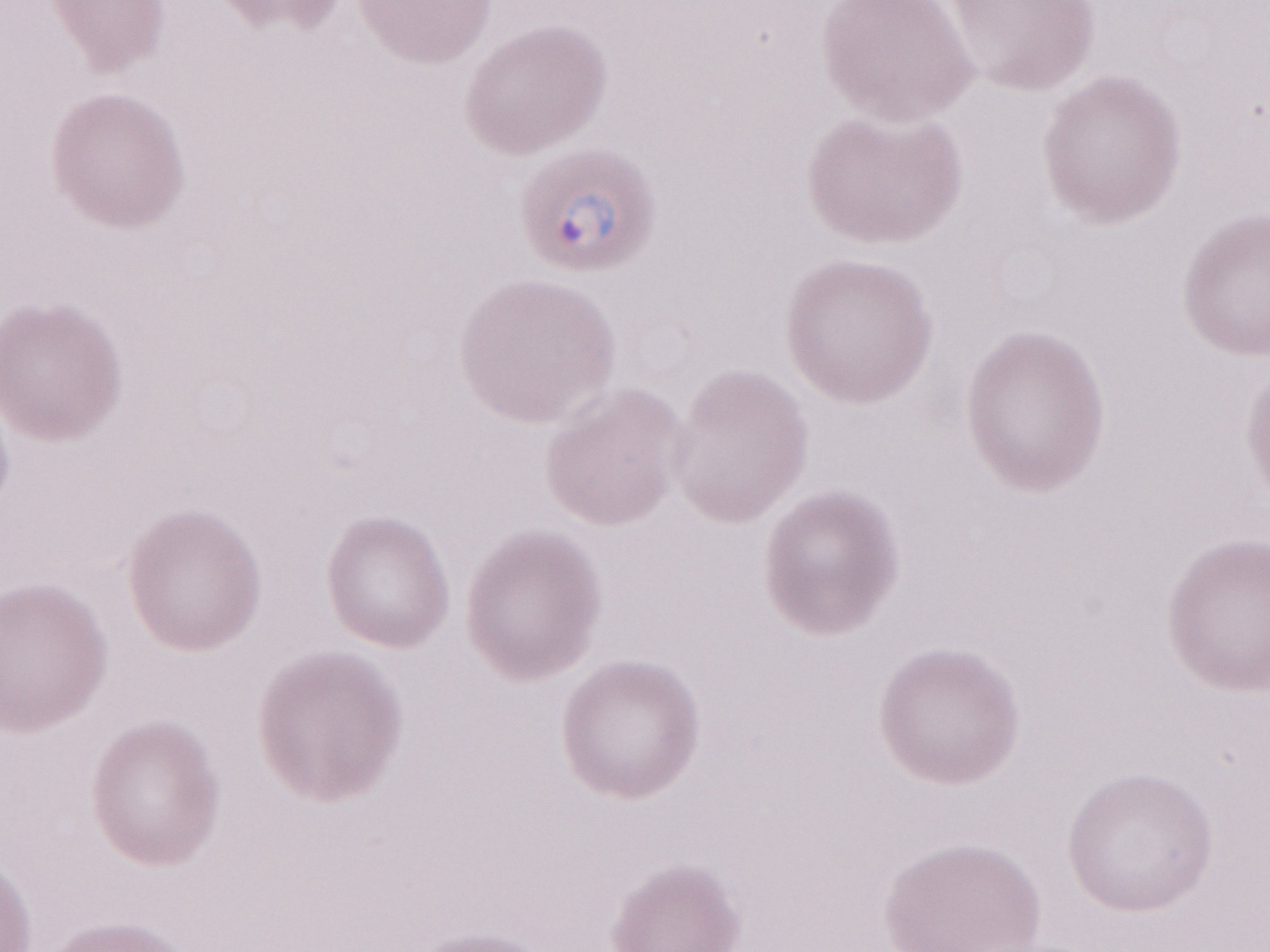

May-Grünwald-Giemsa-stained preparation. Olympus BX43 microscope, Olympus DP73 camera. 1,000x magnification. Single field of view. Image is 1270×952 pixels. Malaria diagnosis (patient-level): positive. Thin peripheral-blood smear.